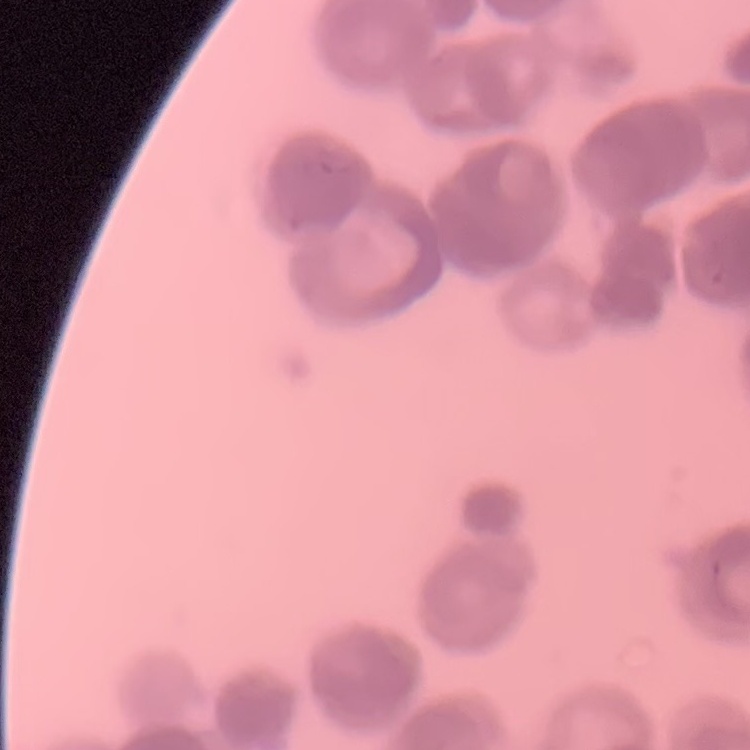

The erythrocytes show rouleaux formation. One tile cut from a larger photomicrograph. Stained with either Field's or Giemsa. Thin peripheral smear.